Classify this cell by malaria status.
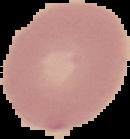

It is uninfected.

Summary:
  - Preparation: thin blood smear
  - Image type: cell region segmented out of the field of view; surrounding area masked to black
  - Image size: 130×139 pixels